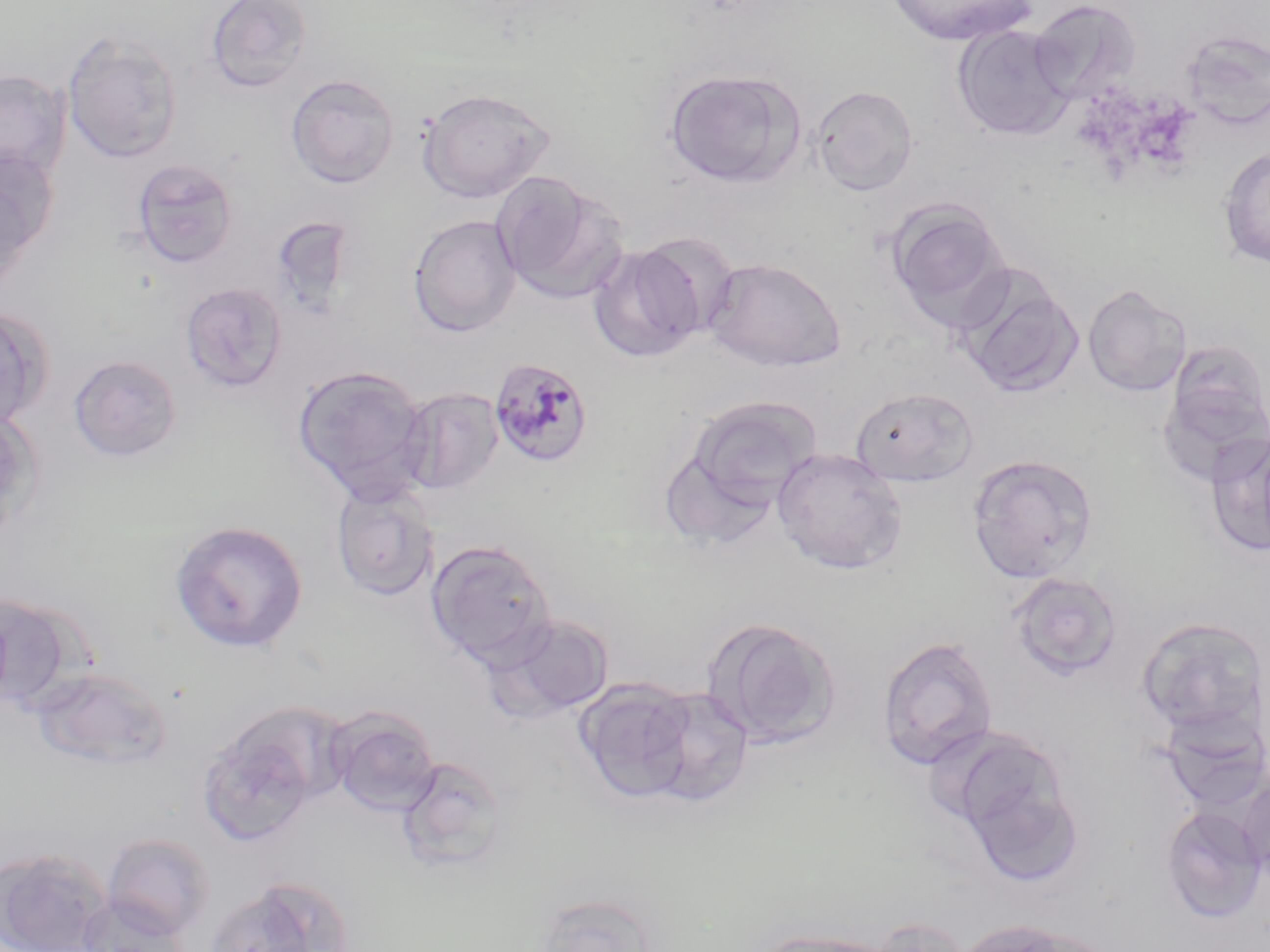

Approximate bounding boxes as (x1,y1)-(x2,y2) corner pairs in pixels. Plasmodium malariae-infected red blood cell locations: (487,356)-(594,468). Uninfected red blood cell locations: (204,0)-(313,93), (885,0)-(1036,46), (1029,0)-(1142,102), (952,25)-(1074,141), (1181,30)-(1269,132), (62,33)-(183,163), (0,69)-(72,183), (664,69)-(806,189), (285,73)-(400,188), (811,84)-(919,196), (417,88)-(555,203), (1218,147)-(1270,268), (0,150)-(56,280), (132,158)-(239,269), (491,171)-(626,303), (0,175)-(33,294), (886,198)-(1013,332), (407,214)-(522,337), (635,232)-(743,342), (588,245)-(705,364), (704,256)-(846,372), (954,266)-(1083,399), (180,281)-(288,394), (1083,283)-(1192,397), (0,306)-(51,431), (68,354)-(182,462), (291,364)-(432,502), (399,387)-(503,495), (850,387)-(979,488), (679,396)-(822,517), (0,408)-(42,541), (1204,430)-(1270,560), (771,447)-(907,574), (967,454)-(1099,584), (331,481)-(440,602), (170,520)-(308,652), (425,538)-(558,669), (1007,572)-(1124,682), (495,613)-(615,718), (1137,616)-(1268,737), (702,617)-(842,749), (876,635)-(998,771), (32,667)-(173,769), (573,677)-(708,803), (326,706)-(441,816), (1158,706)-(1270,812), (197,710)-(330,845), (953,742)-(1084,883), (396,755)-(510,871), (1236,772)-(1270,887), (1161,805)-(1267,923), (101,831)-(216,939), (0,847)-(113,952), (205,876)-(349,952), (533,892)-(658,952), (75,896)-(189,952), (863,916)-(973,952), (950,918)-(1091,952), (752,928)-(893,952). Slide-level diagnosis: Plasmodium malariae. Image is 1270×952 pixels. One field of a larger specimen. Captured at 1000x magnification. Optical microscopy. May-Grünwald-Giemsa-stained preparation. Thin blood film.